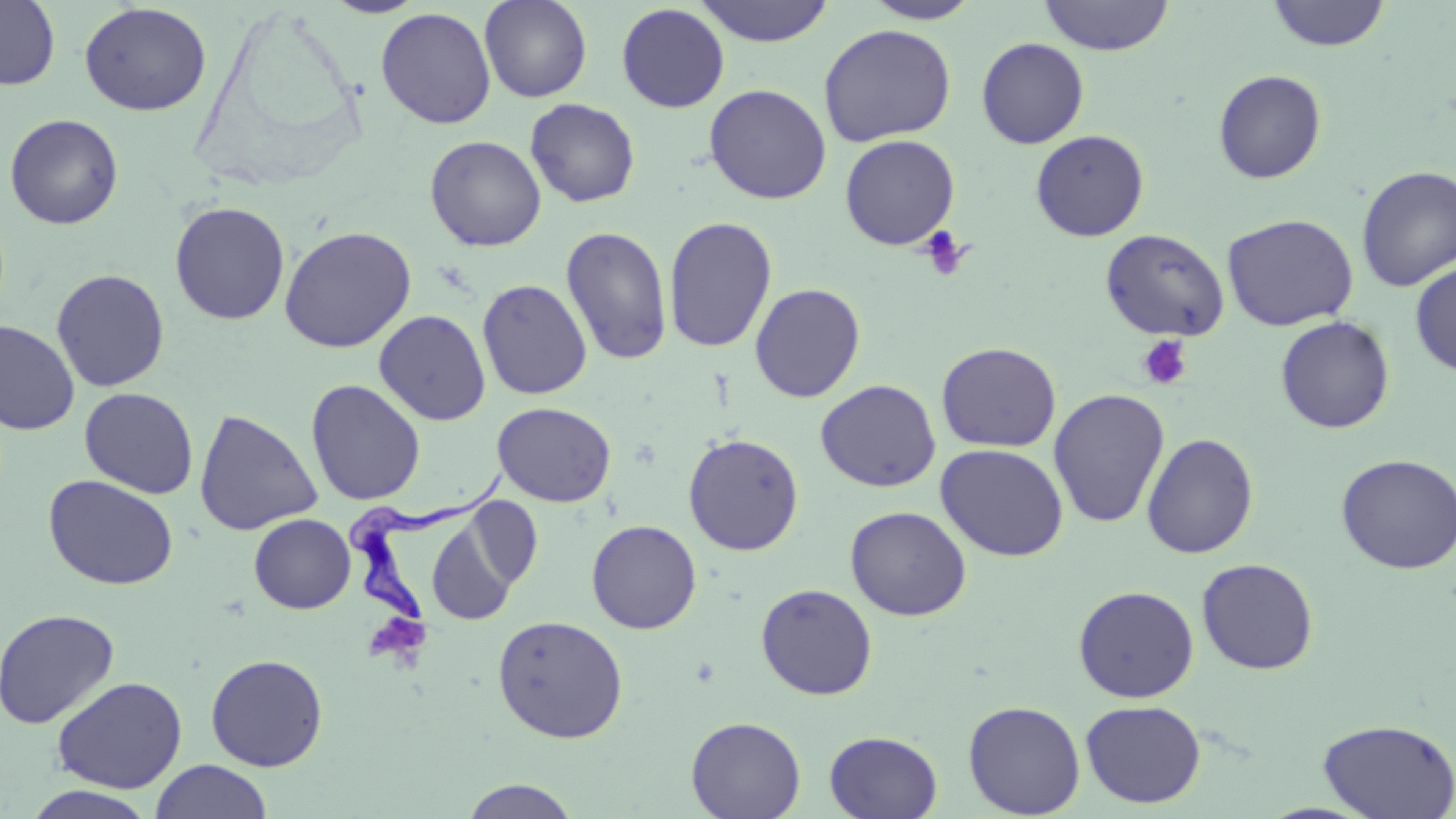 Approximate bounding boxes as named x1/y1/x2/y2 corners in pixels. Platelet locations: (x1=918, y1=226, x2=971, y2=281), (x1=1136, y1=335, x2=1193, y2=390). Uninfected red blood cell locations: (x1=0, y1=0, x2=60, y2=90), (x1=320, y1=0, x2=430, y2=18), (x1=479, y1=0, x2=592, y2=102), (x1=694, y1=0, x2=836, y2=47), (x1=1038, y1=0, x2=1175, y2=55), (x1=862, y1=1, x2=981, y2=24), (x1=1265, y1=1, x2=1391, y2=52), (x1=79, y1=2, x2=212, y2=116), (x1=616, y1=3, x2=730, y2=113), (x1=375, y1=7, x2=496, y2=129), (x1=818, y1=24, x2=957, y2=147), (x1=976, y1=37, x2=1089, y2=148), (x1=1212, y1=69, x2=1327, y2=184), (x1=703, y1=83, x2=832, y2=204), (x1=525, y1=97, x2=641, y2=207), (x1=4, y1=113, x2=124, y2=230), (x1=1030, y1=129, x2=1150, y2=241), (x1=839, y1=134, x2=960, y2=250), (x1=425, y1=135, x2=547, y2=251), (x1=1355, y1=165, x2=1456, y2=292), (x1=170, y1=201, x2=290, y2=325), (x1=1222, y1=213, x2=1359, y2=331), (x1=663, y1=216, x2=778, y2=353), (x1=279, y1=225, x2=417, y2=353), (x1=560, y1=225, x2=673, y2=366), (x1=1100, y1=228, x2=1230, y2=341), (x1=1409, y1=261, x2=1456, y2=377), (x1=51, y1=269, x2=170, y2=392), (x1=476, y1=278, x2=592, y2=400), (x1=749, y1=282, x2=866, y2=402), (x1=373, y1=309, x2=491, y2=426), (x1=1274, y1=315, x2=1395, y2=434), (x1=0, y1=321, x2=80, y2=435), (x1=936, y1=341, x2=1061, y2=452), (x1=305, y1=379, x2=426, y2=506), (x1=815, y1=379, x2=941, y2=492), (x1=79, y1=387, x2=199, y2=499), (x1=1048, y1=389, x2=1170, y2=529), (x1=492, y1=402, x2=617, y2=507), (x1=193, y1=408, x2=323, y2=536), (x1=683, y1=433, x2=804, y2=556), (x1=1141, y1=433, x2=1259, y2=559), (x1=936, y1=443, x2=1069, y2=562), (x1=1336, y1=453, x2=1456, y2=575), (x1=42, y1=473, x2=180, y2=591), (x1=463, y1=496, x2=544, y2=593), (x1=845, y1=505, x2=971, y2=621), (x1=249, y1=513, x2=356, y2=613), (x1=426, y1=519, x2=520, y2=625), (x1=586, y1=519, x2=702, y2=634), (x1=1196, y1=557, x2=1319, y2=675), (x1=755, y1=583, x2=878, y2=700), (x1=1073, y1=585, x2=1199, y2=703), (x1=0, y1=608, x2=120, y2=729), (x1=491, y1=615, x2=628, y2=743), (x1=205, y1=653, x2=329, y2=772), (x1=51, y1=675, x2=187, y2=794), (x1=1080, y1=699, x2=1206, y2=808), (x1=963, y1=700, x2=1085, y2=818), (x1=686, y1=716, x2=806, y2=819), (x1=1318, y1=716, x2=1456, y2=819), (x1=824, y1=730, x2=943, y2=818), (x1=151, y1=760, x2=271, y2=819), (x1=457, y1=778, x2=582, y2=818), (x1=20, y1=785, x2=159, y2=819). Trypanosoma brucei locations: (x1=340, y1=471, x2=507, y2=629). Slide-level diagnosis: Trypanosoma brucei. Captured at 1000x magnification. Single field of view. Optical microscopy. Thin blood film. Image is 1456×819 pixels. May-Grünwald-Giemsa-stained preparation.